State the preparation type.
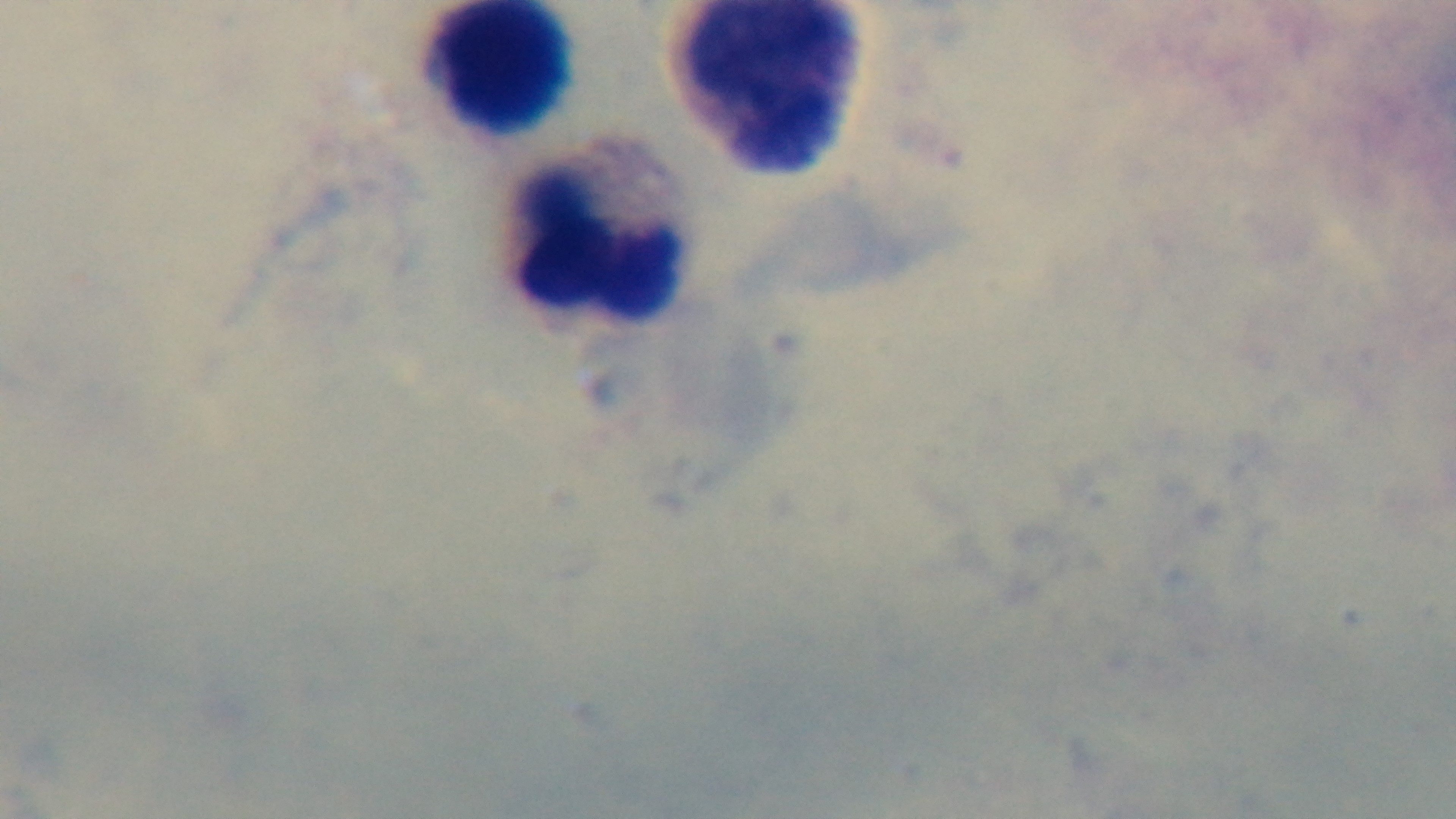
Thick.

Summary:
  - Stain: Giemsa
  - Modality: light microscopy
  - Field of view: one from the slide
  - Objective: 100x oil immersion
  - Malaria status: uninfected
  - Capture: mounted 4K digital camera